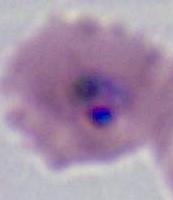

A Plasmodium parasite is seen. Photomicrograph. Captured at either 400x or 1000x magnification.